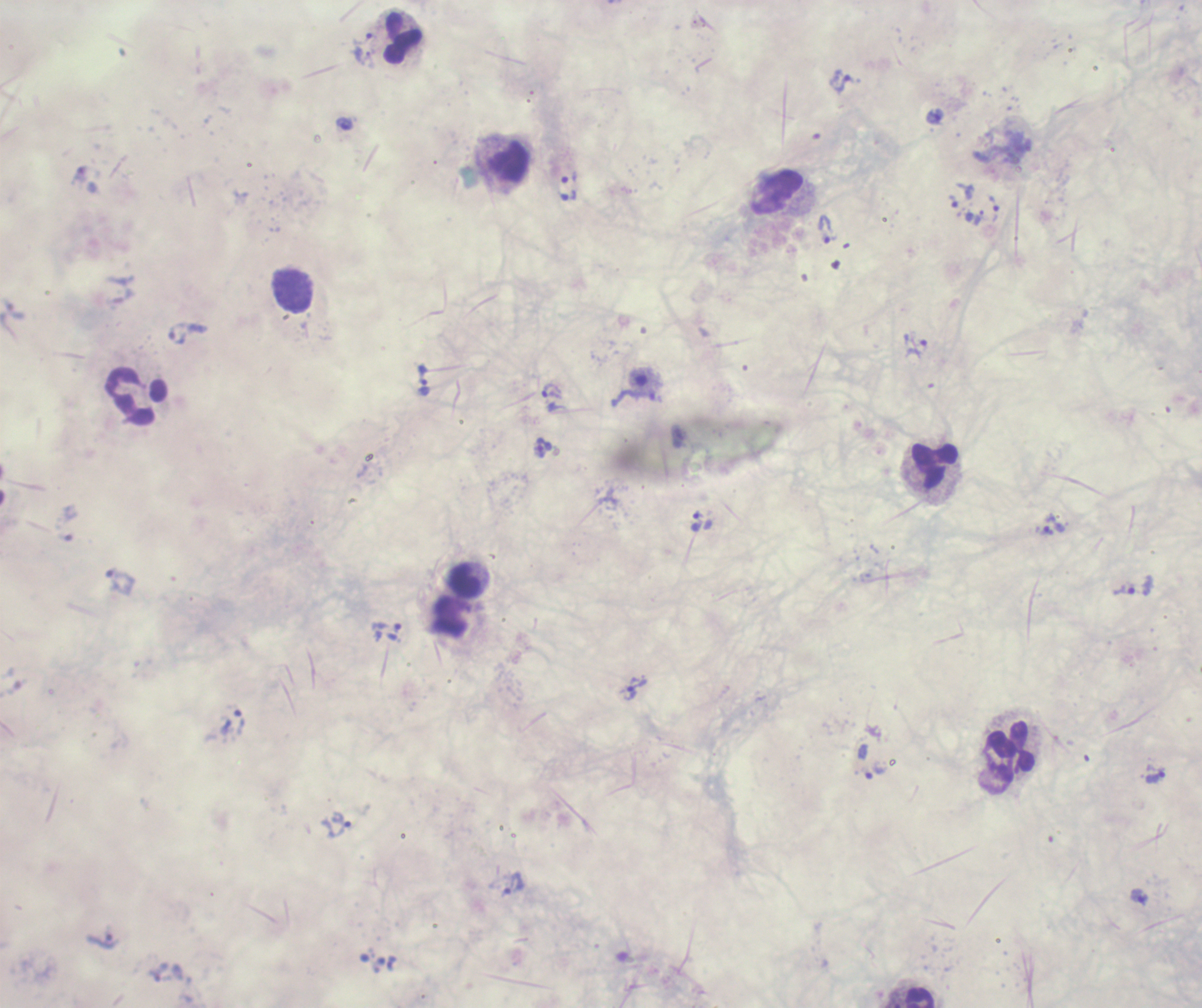

coordinate format = approximate object centers, in pixels from the top-left corner
leukocyte locations = (x=402, y=38), (x=508, y=161), (x=777, y=192), (x=136, y=396), (x=934, y=465), (x=465, y=581), (x=1011, y=751), (x=920, y=997)
trophozoite locations = (x=366, y=39), (x=842, y=82), (x=569, y=177), (x=954, y=201), (x=993, y=208), (x=828, y=229), (x=187, y=334), (x=917, y=347), (x=425, y=379), (x=552, y=392), (x=544, y=447), (x=697, y=520), (x=1055, y=524), (x=119, y=581), (x=1123, y=588), (x=386, y=626), (x=637, y=689), (x=239, y=721), (x=876, y=772), (x=1155, y=778), (x=338, y=825), (x=514, y=883), (x=1138, y=896)
preparation = thick blood smear
result = malaria parasites identified
stain = Romanowsky
field of view = one from this slide
coloration quality = bad
image size = 1202×1008 pixels
magnification = 100x
background quality = poor
context = previously used in an actual diagnosis